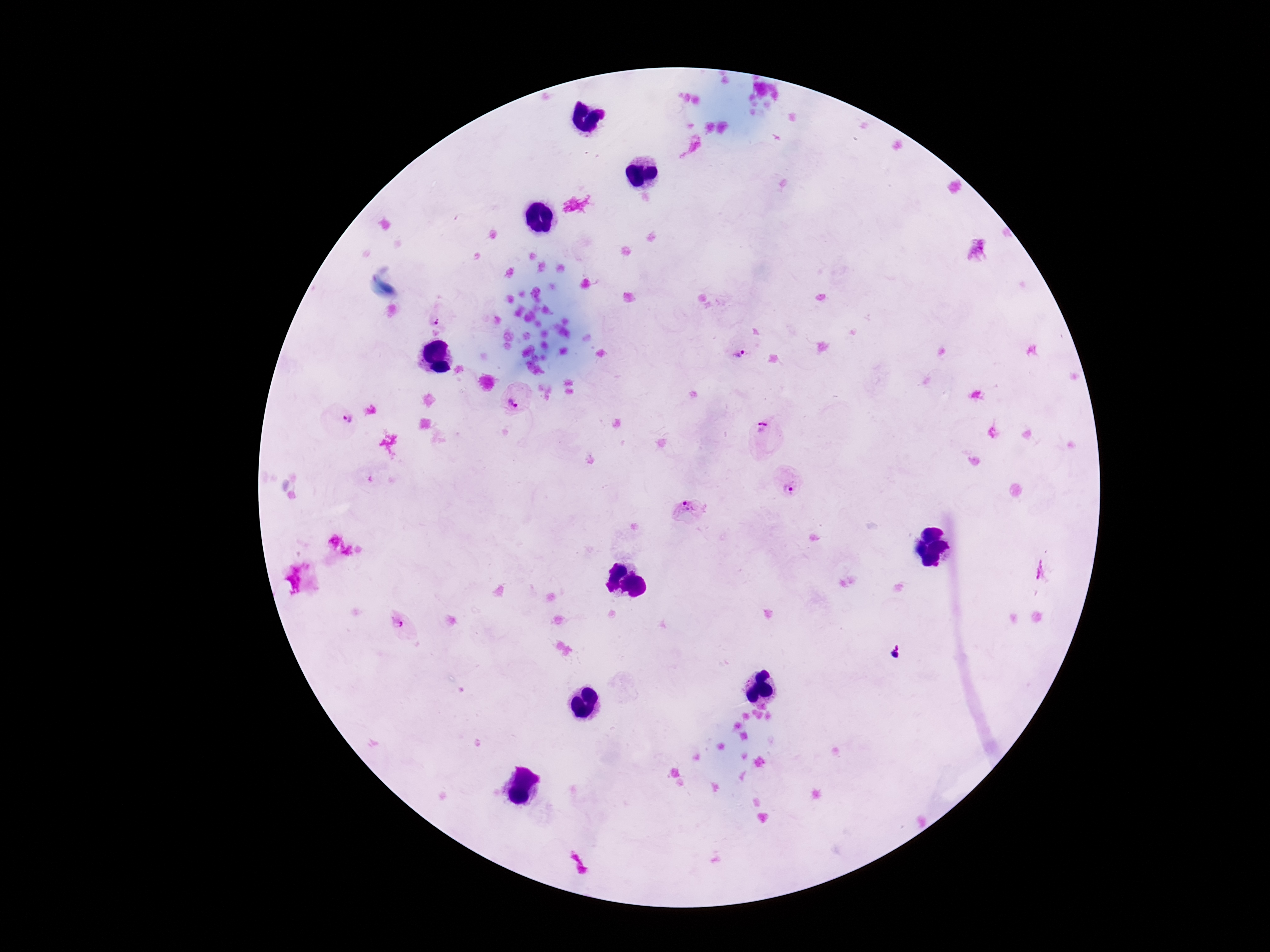 Approximate centers as {x, y} in pixels. Plasmodium parasite locations: {440, 315}, {738, 353}, {516, 402}, {341, 419}, {764, 434}, {790, 484}, {690, 512}, {1039, 570}, {404, 625}, {896, 652}. Patient malaria status: positive. Image is 1270×952 pixels. 100x magnification. One field from this slide. Giemsa-stained preparation. Thick blood film. Smartphone photograph taken through the microscope eyepiece.